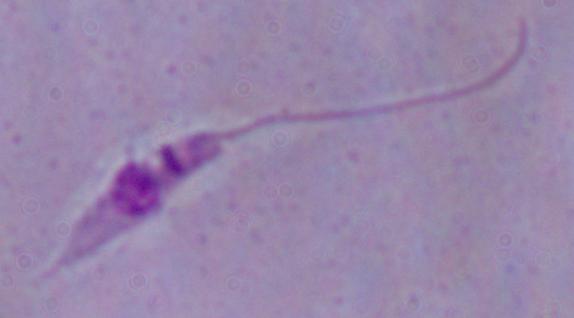

magnification = 1000x
modality = photomicrograph
identification = Leishmania